Report the malaria status of this cell.
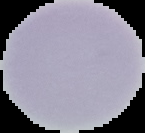
Uninfected.

image type = segmented cell region on a black background
image size = 145×133 pixels
preparation = thin blood film